Assess this cell for malaria.
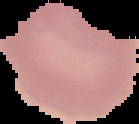

It is uninfected.

Summary:
  - Preparation: thin blood film
  - Image size: 139×124 pixels
  - Image type: cell region segmented out of the field of view; surrounding area masked to black